Name the parasite shown.
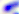

Toxoplasma gondii.

modality = photomicrograph
magnification = 400x